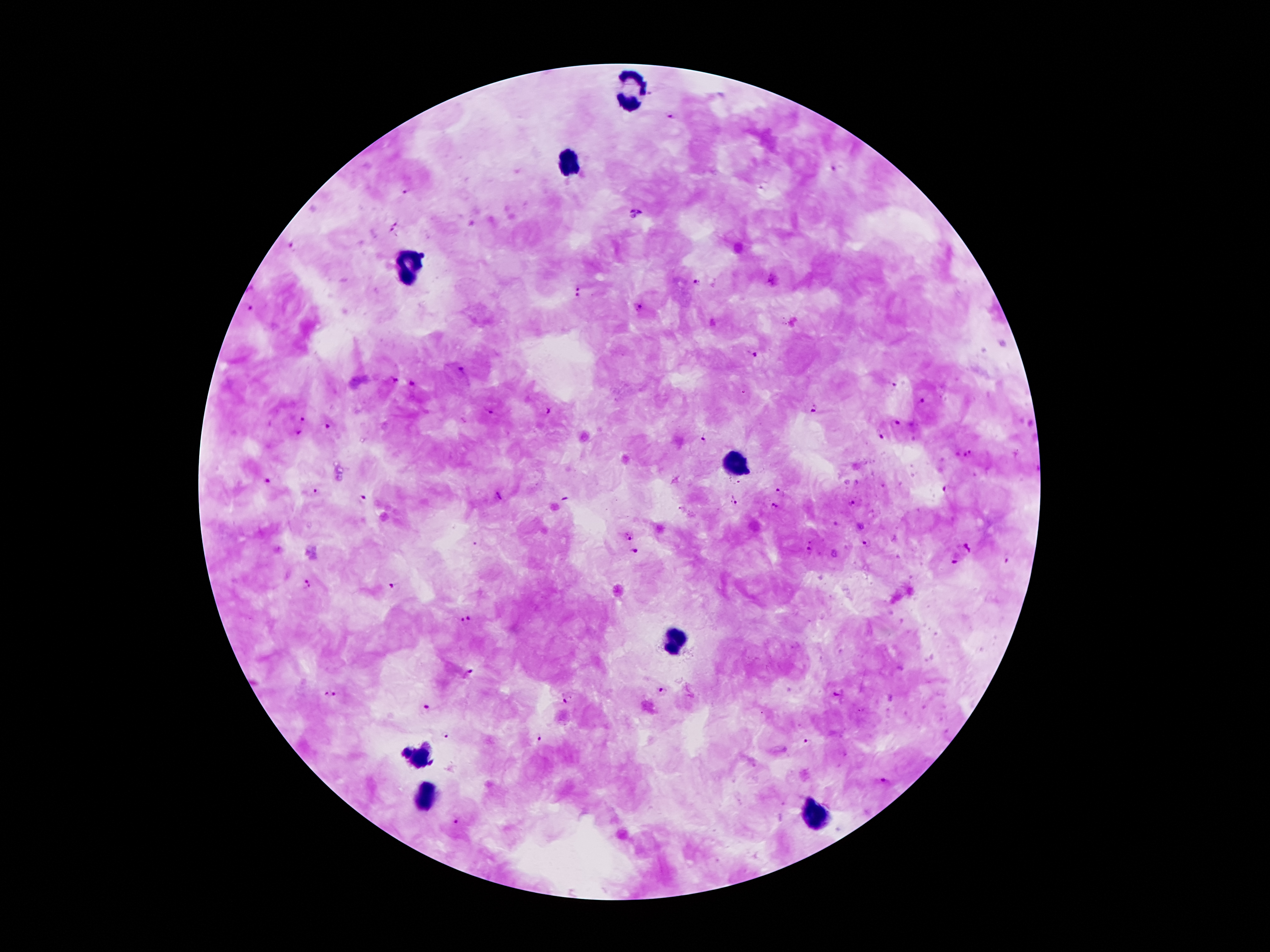

Approximate object centers, in pixels from the top-left corner. Plasmodium parasite locations: (x=668, y=116), (x=834, y=170), (x=759, y=187), (x=406, y=191), (x=636, y=214), (x=394, y=220), (x=390, y=232), (x=291, y=244), (x=698, y=283), (x=580, y=287), (x=578, y=298), (x=638, y=306), (x=251, y=310), (x=753, y=355), (x=462, y=369), (x=396, y=381), (x=413, y=384), (x=893, y=384), (x=923, y=399), (x=812, y=410), (x=490, y=412), (x=548, y=412), (x=302, y=419), (x=897, y=420), (x=328, y=427), (x=300, y=432), (x=881, y=436), (x=703, y=440), (x=967, y=453), (x=267, y=481), (x=945, y=489), (x=779, y=491), (x=315, y=492), (x=362, y=497), (x=733, y=501), (x=851, y=503), (x=775, y=506), (x=627, y=535), (x=811, y=539), (x=865, y=544), (x=967, y=549), (x=807, y=551), (x=636, y=552), (x=1008, y=560), (x=954, y=563), (x=306, y=585), (x=393, y=586), (x=467, y=619), (x=468, y=671), (x=664, y=691), (x=329, y=695), (x=837, y=695), (x=567, y=700), (x=427, y=707), (x=446, y=735), (x=538, y=739), (x=807, y=744), (x=885, y=780), (x=456, y=821). Leukocyte locations: (x=627, y=89), (x=571, y=165), (x=413, y=266), (x=735, y=466), (x=672, y=643), (x=424, y=757), (x=426, y=796), (x=817, y=819). Patient malaria status: positive for Plasmodium falciparum. Thick blood film. Giemsa-stained preparation. 100x magnification. Smartphone photograph taken through the microscope eyepiece. One field from this slide. Image is 1270×952 pixels.